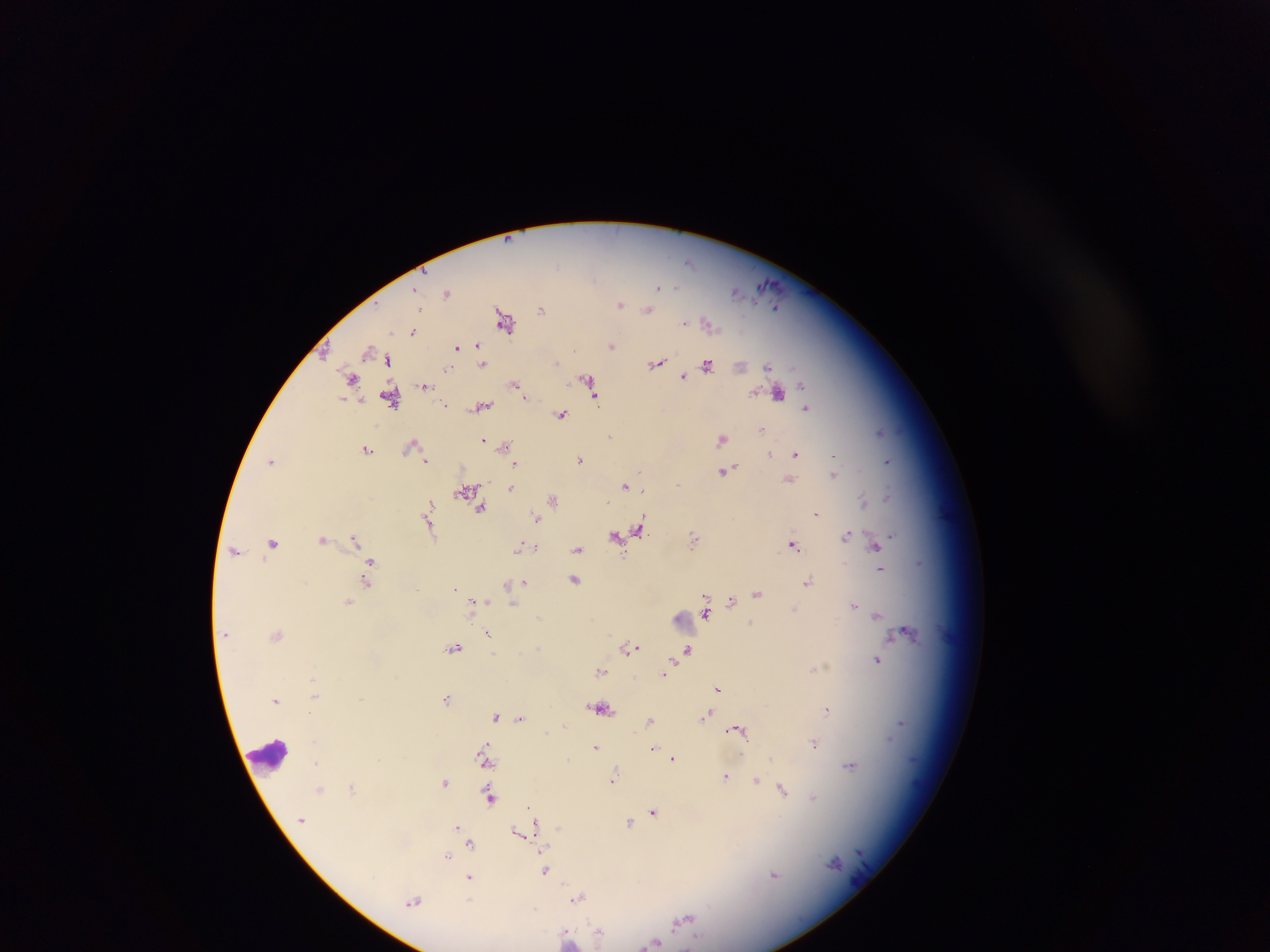

malaria parasite locations = approximate centers as [x, y] in pixels: [689, 261], [659, 286], [676, 287], [737, 291], [447, 293], [620, 304], [776, 307], [541, 309], [648, 310], [504, 320], [683, 322], [708, 323], [412, 332], [612, 345], [480, 347], [457, 348], [367, 351], [388, 359], [556, 363], [657, 363], [483, 364], [707, 365], [740, 366], [767, 367], [448, 369], [683, 376], [351, 379], [587, 381], [515, 384], [425, 385], [591, 390], [778, 393], [594, 397], [390, 398], [445, 405], [480, 407], [807, 409], [561, 415], [762, 430], [880, 431], [611, 436], [722, 439], [483, 440], [505, 446], [415, 447], [368, 449], [795, 453], [770, 454], [580, 459], [272, 460], [426, 461], [889, 461], [516, 464], [726, 471], [833, 474], [789, 480], [625, 486], [511, 487], [643, 490], [466, 491], [888, 496], [554, 500], [864, 501], [429, 506], [482, 509], [816, 514], [429, 517], [536, 517], [639, 530], [628, 532], [847, 535], [892, 535], [616, 537], [355, 538], [695, 539], [323, 540], [274, 543], [875, 544], [793, 545], [520, 546], [577, 549], [235, 551], [370, 562], [921, 562], [370, 568], [881, 569], [574, 579], [367, 581], [808, 581], [524, 582], [508, 584], [455, 588], [757, 594], [731, 601], [348, 602], [473, 603], [513, 605], [854, 606], [794, 608], [705, 613], [877, 616], [539, 617], [907, 632], [226, 633], [488, 634], [278, 635], [454, 648], [538, 648], [631, 648], [688, 649], [877, 660], [814, 668], [601, 671], [664, 672], [718, 689], [315, 693], [446, 698], [276, 700], [601, 708], [827, 709], [707, 714], [496, 716], [521, 718], [650, 720], [901, 723], [737, 729], [547, 732], [814, 743], [596, 747], [652, 749], [673, 759], [568, 760], [485, 761], [316, 763], [850, 766], [614, 777], [725, 777], [756, 781], [445, 782], [772, 786], [352, 788], [321, 789], [783, 790], [490, 797], [813, 798], [529, 808], [653, 812], [640, 817], [535, 821], [630, 823], [458, 827], [519, 832], [467, 837], [470, 843], [448, 855], [834, 862], [545, 871], [774, 875], [470, 878], [578, 898], [469, 900], [414, 901], [685, 920], [599, 933], [567, 938], [653, 942]
country = Ghana
preparation = thick blood smear
field of view = single
capture = mobile-phone photograph through a microscope
image size = 1270×952 pixels
leukocyte locations = approximate centers as [x, y] in pixels: [686, 622], [269, 756]